Mark where platelets are.
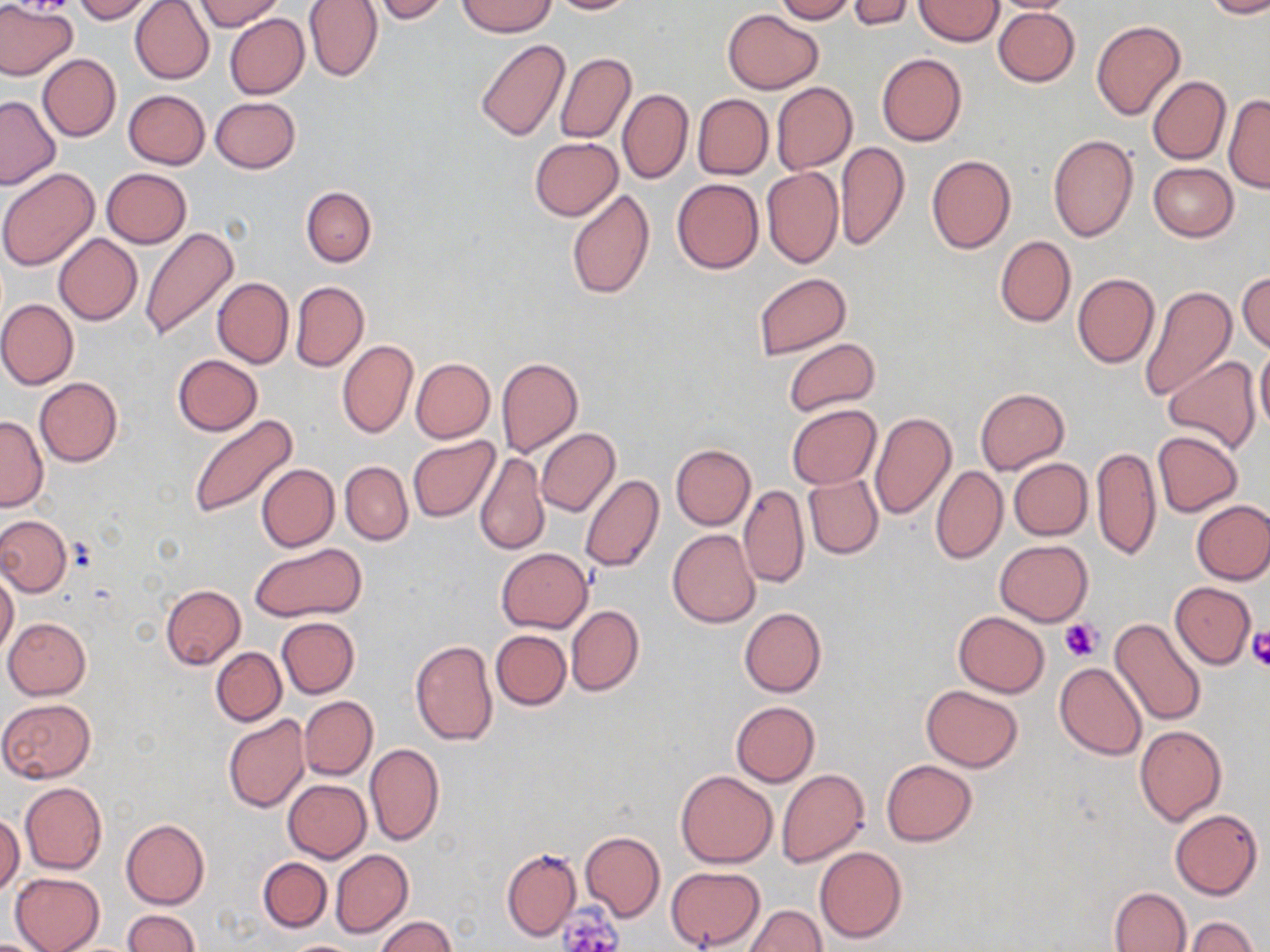

Approximate bounding boxes as (x1, y1, x2, y2) in pixels.
Platelets: (1059, 618, 1102, 660), (1246, 627, 1270, 671), (556, 905, 623, 951).

slide-level diagnosis = negative for blood parasites
preparation = thin blood smear
uninfected red blood cell locations = approximate bounding boxes as (x1, y1, x2, y2) in pixels: (0, 0, 77, 81), (74, 0, 155, 22), (130, 0, 214, 84), (195, 0, 283, 31), (303, 0, 383, 82), (372, 0, 449, 23), (546, 0, 639, 14), (773, 0, 857, 23), (846, 0, 914, 30), (914, 0, 1003, 46), (985, 0, 1084, 14), (1203, 0, 1270, 20), (457, 1, 556, 37), (992, 5, 1079, 86), (722, 9, 823, 94), (224, 13, 308, 99), (1090, 19, 1186, 121), (475, 40, 569, 141), (555, 52, 636, 145), (877, 52, 966, 147), (38, 53, 120, 141), (1148, 75, 1231, 165), (771, 82, 857, 174), (618, 88, 693, 184), (123, 89, 209, 169), (692, 94, 773, 178), (1223, 95, 1269, 192), (0, 96, 60, 189), (211, 97, 300, 173), (1048, 135, 1137, 241), (529, 137, 622, 220), (836, 142, 910, 250), (927, 154, 1016, 254), (1149, 163, 1239, 242), (762, 167, 843, 268), (101, 168, 192, 247), (0, 169, 99, 271), (672, 178, 763, 274), (301, 186, 376, 266), (566, 189, 655, 300), (139, 226, 240, 341), (54, 234, 143, 325), (995, 235, 1076, 327), (1237, 272, 1270, 353), (754, 273, 851, 357), (1073, 273, 1159, 369), (212, 276, 293, 368), (289, 280, 368, 372), (1136, 284, 1235, 402), (0, 299, 78, 389), (783, 338, 881, 417), (337, 339, 417, 439), (1255, 340, 1270, 439), (173, 354, 263, 435), (1164, 356, 1261, 454), (410, 358, 494, 443), (496, 358, 583, 459), (34, 377, 122, 467), (975, 387, 1069, 473), (787, 404, 881, 488), (869, 412, 956, 520), (187, 414, 298, 519), (0, 415, 48, 511), (534, 428, 620, 517), (1152, 430, 1243, 516), (407, 437, 500, 522), (670, 444, 756, 531), (1091, 445, 1161, 561), (476, 451, 549, 556), (1009, 458, 1092, 540), (339, 462, 413, 545), (256, 463, 338, 552), (931, 465, 1008, 564), (804, 473, 883, 559), (580, 474, 664, 574), (738, 484, 808, 589), (1192, 501, 1270, 584), (0, 515, 71, 597), (667, 529, 761, 628), (994, 539, 1093, 626), (250, 542, 367, 622), (496, 549, 592, 632), (0, 571, 19, 659), (1169, 581, 1255, 668), (160, 585, 245, 669), (566, 606, 643, 696), (739, 606, 826, 697), (953, 611, 1050, 697), (1109, 616, 1207, 726), (2, 617, 92, 699), (277, 618, 359, 698), (490, 629, 571, 710), (410, 639, 498, 746), (211, 648, 286, 725), (1055, 661, 1147, 760), (920, 685, 1023, 772), (299, 696, 377, 780), (1, 698, 97, 783), (730, 700, 820, 786), (222, 714, 309, 812), (1134, 725, 1226, 824), (364, 743, 445, 847), (881, 759, 976, 846), (776, 769, 870, 868), (675, 771, 777, 868), (283, 780, 371, 863), (20, 782, 107, 875), (1169, 809, 1262, 899), (0, 813, 24, 897), (120, 818, 209, 909), (580, 831, 665, 923), (815, 846, 907, 944), (501, 848, 581, 940), (329, 849, 412, 938), (258, 856, 332, 933), (666, 866, 765, 950), (10, 872, 105, 952), (1109, 887, 1190, 952), (744, 905, 828, 951), (123, 910, 198, 952), (373, 915, 456, 952), (1184, 916, 1259, 952), (281, 939, 362, 951)
stain = May-Grünwald-Giemsa
field of view = one of a larger specimen
image size = 1270×952 pixels
modality = light microscopy
magnification = 1000x